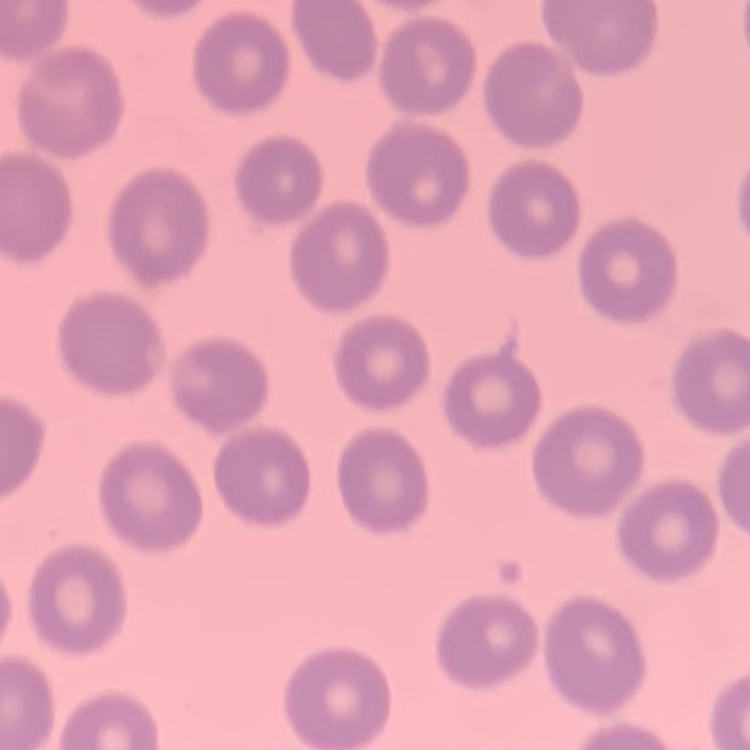
The erythrocytes show no rouleaux formation. Thin blood smear. Stained with either Field's or Giemsa. One tile cut from a larger photomicrograph.